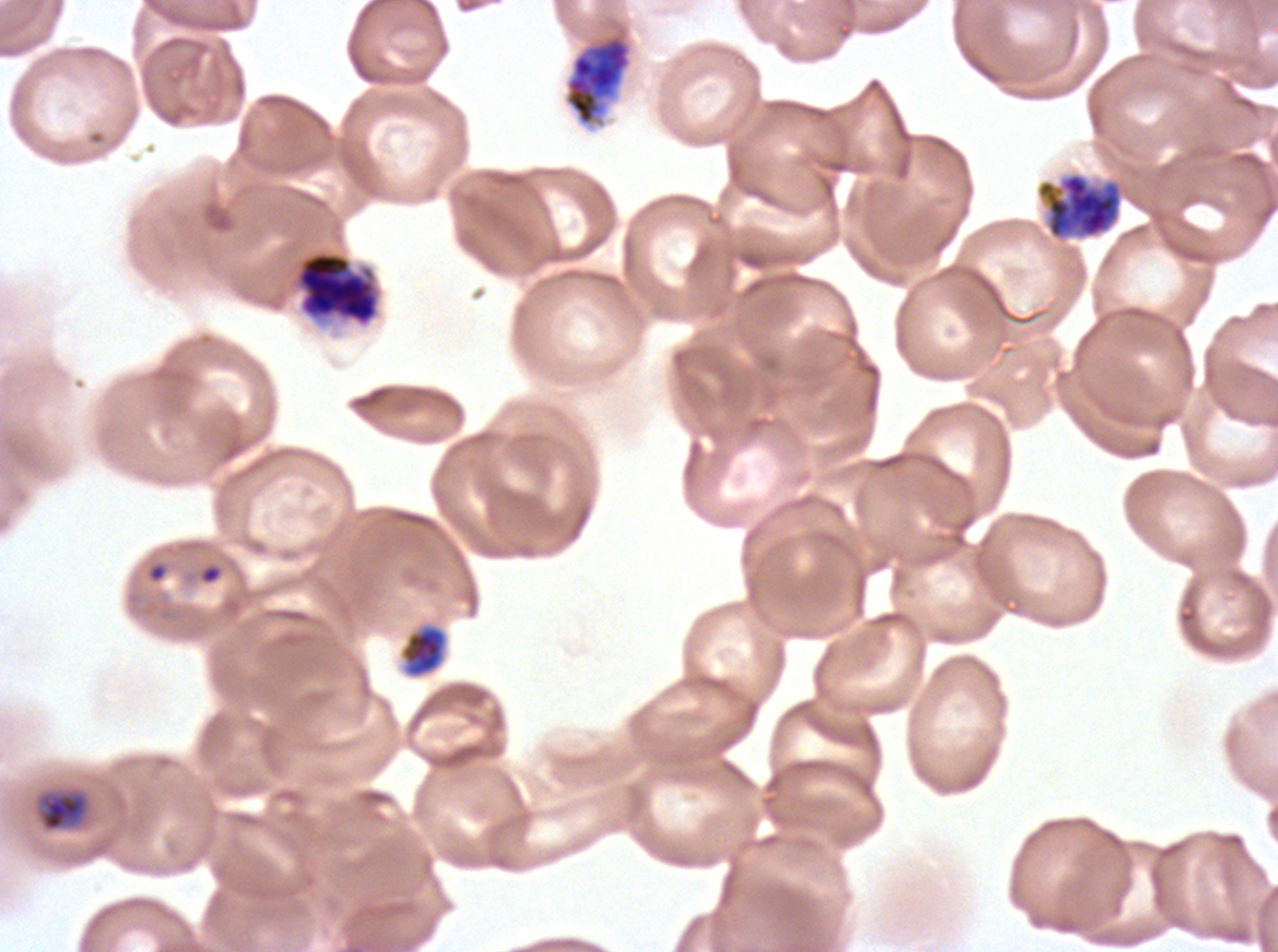
field_of_view: sub-image separated from a larger composite
specimen: P. falciparum from a patient in The Gambia, cultured ex vivo for 24 to 48 hours
late_schizont_locations: 'approximate bounding boxes as {x1, y1, x2, y2} in pixels: {564, 33, 632, 126}'
debris_locations: 'approximate bounding boxes as {x1, y1, x2, y2} in pixels: {146, 561, 169, 584}'
early_schizont_locations: 'approximate bounding boxes as {x1, y1, x2, y2} in pixels: {1048, 174, 1120, 238}, {295, 251, 379, 326}, {399, 624, 448, 678}'
stain: Giemsa
image_size: 1278×952 pixels
ring_locations: 'approximate bounding boxes as {x1, y1, x2, y2} in pixels: {198, 563, 223, 585}'
preparation: thin blood smear
late_ring_early_trophozoite_locations: 'approximate bounding boxes as {x1, y1, x2, y2} in pixels: {40, 793, 88, 831}'
life_cycle_stages_observed: ring, late-ring/early-trophozoite, early schizont, late schizont